Report the malaria status of this cell.
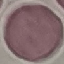
It is uninfected.

Thin blood smear. Giemsa stain. Photographed with a smartphone camera at the microscope eyepiece. Automatically extracted cell patch, resized to 64 × 64 pixels.